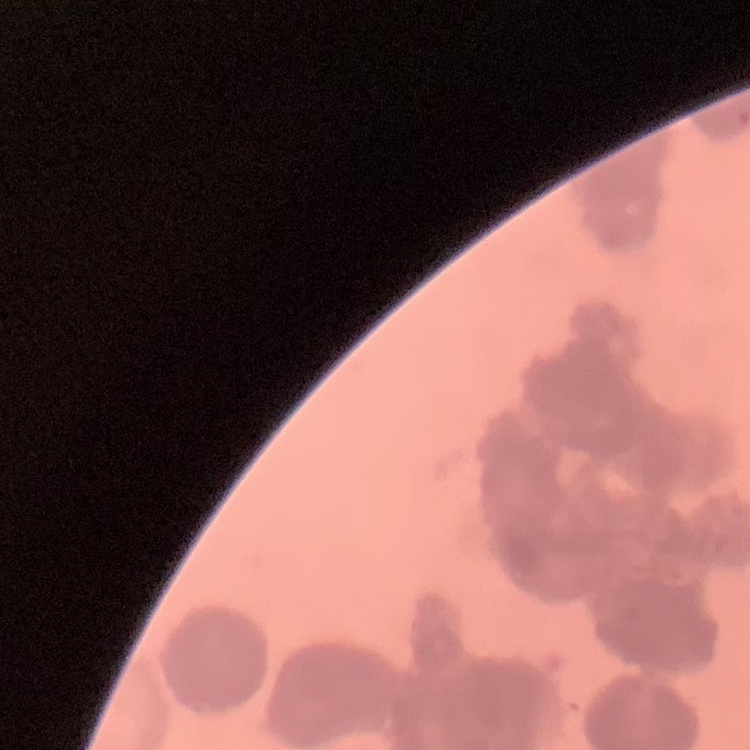

{
  "red_blood_cell_morphology": "rouleaux formation",
  "stain": "Field's or Giemsa",
  "preparation": "thin blood film",
  "image_type": "square crop of a larger photomicrograph"
}